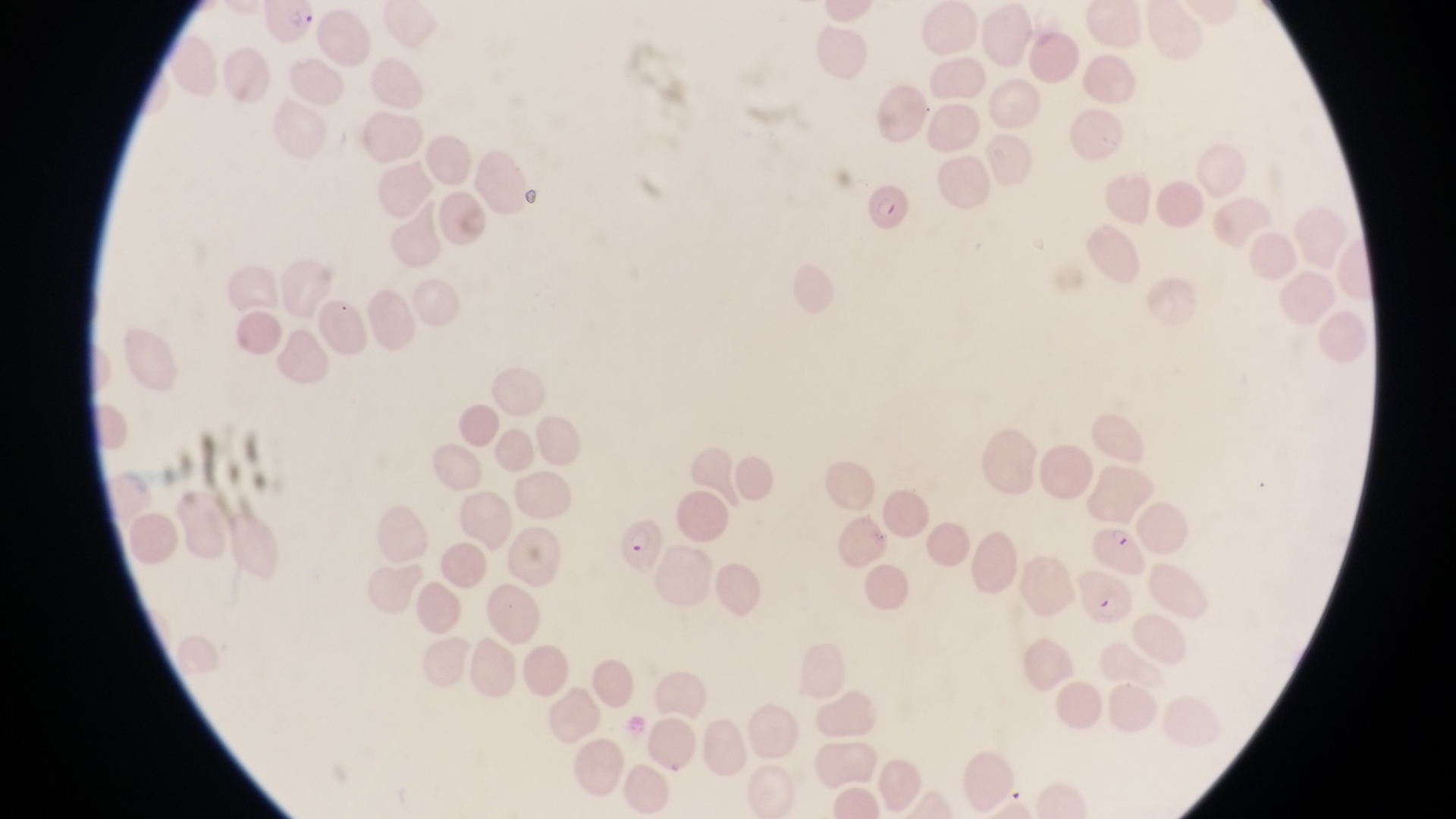

Approximate bounding boxes as [left, top, right, bottom] in pixels. Parasitised red blood cell locations: [264, 2, 323, 47], [861, 180, 913, 235], [617, 512, 669, 573], [1096, 523, 1146, 572]. Single field of view. At a magnification of 1000x. Thin blood film. Collected in Uganda. Photographed through the eyepiece of an Olympus CX-23 microscope with a smartphone camera. Image is 1456×819 pixels.